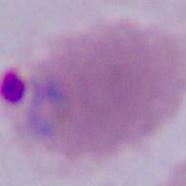 Captured at either 400x or 1000x magnification. A Plasmodium parasite is shown. Micrograph.